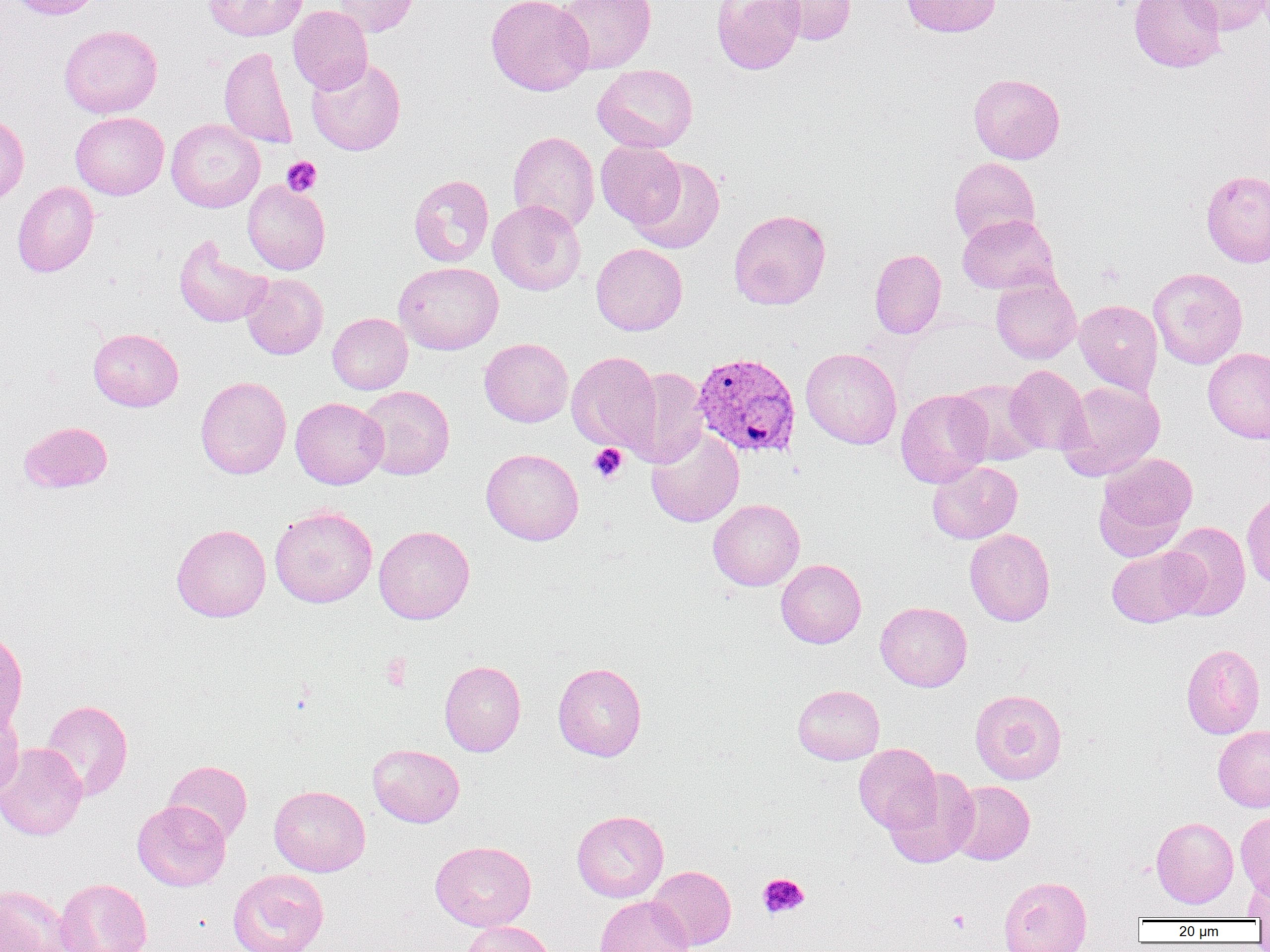
slide-level diagnosis = Plasmodium vivax
image size = 1270×952 pixels
field of view = single
uninfected red blood cell locations = approximate bounding boxes as (x1,y1)-(x2,y2) corner pairs in pixels: (8,0)-(102,19), (203,0)-(307,41), (332,0)-(418,37), (486,0)-(594,95), (556,0)-(656,73), (711,0)-(805,75), (769,0)-(856,45), (901,0)-(1001,37), (1129,0)-(1227,73), (1176,0)-(1270,35), (288,5)-(372,93), (59,25)-(162,118), (219,46)-(298,149), (306,57)-(406,155), (593,63)-(698,153), (968,72)-(1065,164), (70,111)-(169,199), (0,114)-(29,203), (166,119)-(265,212), (508,130)-(599,233), (596,141)-(685,229), (629,156)-(725,254), (949,157)-(1041,245), (1201,169)-(1270,268), (408,175)-(494,268), (242,180)-(330,275), (12,181)-(98,277), (488,200)-(585,295), (728,209)-(831,310), (957,214)-(1059,294), (174,234)-(270,328), (591,243)-(687,335), (869,248)-(946,339), (394,262)-(503,354), (1148,267)-(1248,369), (241,273)-(328,359), (991,273)-(1081,365), (1074,299)-(1163,395), (327,313)-(412,394), (88,328)-(183,411), (480,338)-(573,427), (800,347)-(902,449), (1202,348)-(1270,443), (567,351)-(660,452), (1005,365)-(1091,455), (623,368)-(710,468), (195,376)-(291,479), (950,379)-(1045,466), (1056,380)-(1165,481), (357,385)-(455,480), (895,388)-(993,488), (290,397)-(388,489), (19,421)-(112,492), (646,427)-(744,527), (481,448)-(584,545), (1094,450)-(1197,555), (927,461)-(1022,543), (1242,491)-(1270,590), (708,499)-(804,590), (269,505)-(378,608), (1161,522)-(1251,620), (171,524)-(271,622), (374,525)-(475,624), (965,528)-(1055,626), (1106,546)-(1205,627), (776,559)-(866,648), (875,602)-(972,692), (0,629)-(28,733), (1181,644)-(1265,738), (439,660)-(526,756), (553,662)-(646,761), (793,684)-(884,765), (970,689)-(1067,784), (40,699)-(133,801), (0,703)-(24,799), (1213,724)-(1270,812), (0,743)-(87,841), (853,743)-(941,833), (368,744)-(465,827), (163,760)-(252,845), (883,768)-(979,868), (949,781)-(1034,865), (268,785)-(370,876), (132,800)-(231,891), (571,810)-(668,902), (1235,810)-(1270,897), (1151,816)-(1238,908), (430,840)-(536,931), (647,865)-(736,950), (227,868)-(329,952), (1243,870)-(1270,921), (999,876)-(1092,952), (53,878)-(151,952), (0,885)-(71,951), (594,895)-(694,952), (461,921)-(556,952)
platelet locations = approximate bounding boxes as (x1,y1)-(x2,y2) corner pairs in pixels: (282,157)-(322,196), (589,444)-(627,483), (381,653)-(412,690), (758,873)-(809,918), (946,910)-(971,933)
preparation = thin blood smear
magnification = 1000x
modality = optical microscopy
Plasmodium vivax-infected red blood cell locations = approximate bounding boxes as (x1,y1)-(x2,y2) corner pairs in pixels: (692,351)-(802,458)